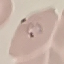
{
  "result": "malaria parasites detected",
  "capture": "smartphone through the microscope eyepiece",
  "preparation": "thin smear",
  "stain": "Giemsa",
  "image_type": "automatically extracted cell patch, resized to 64 × 64 pixels"
}